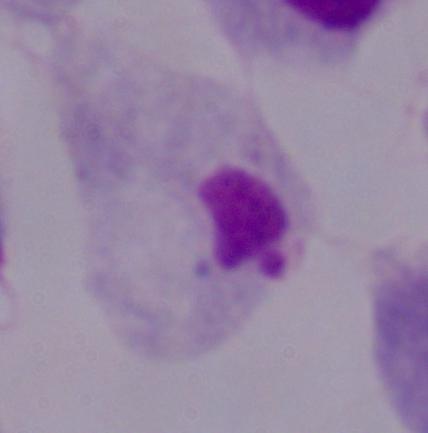
{
  "modality": "micrograph",
  "identification": "trichomonad",
  "magnification": "1000x"
}